Comment on the morphology of the red blood cells.
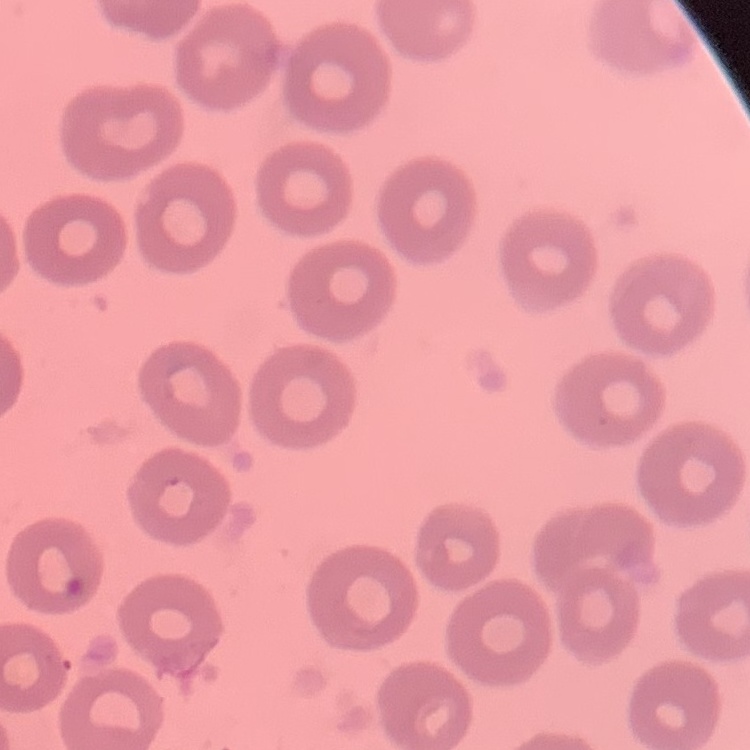
They show no rouleaux formation.

Summary:
  - Image type: square crop of a larger photomicrograph
  - Stain: Field's or Giemsa
  - Preparation: thin peripheral smear